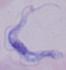

Summary:
  - Magnification: 1000x
  - Identification: trypanosome
  - Modality: photomicrograph